Outline each uninfected red blood cell.
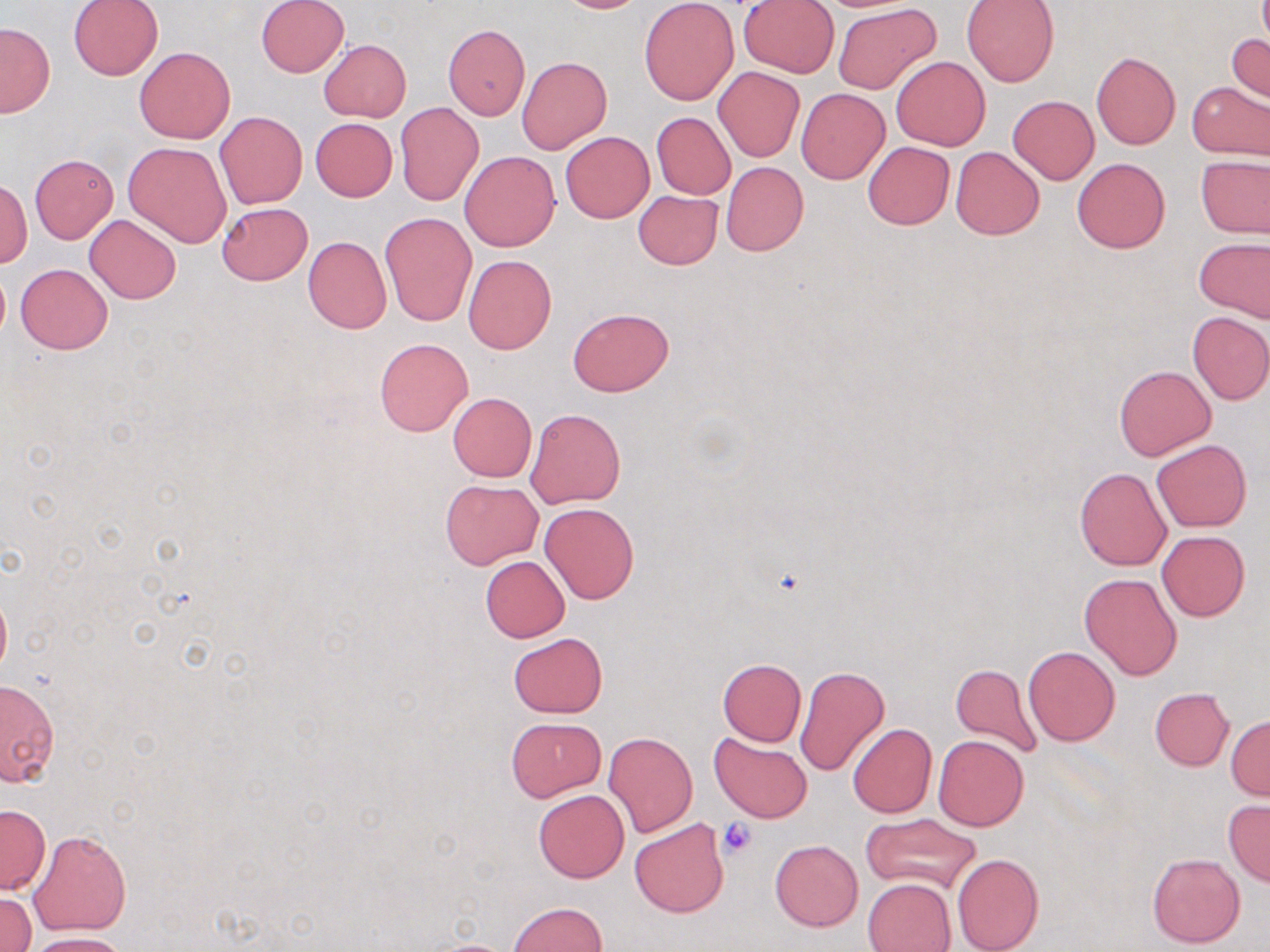
Approximate bounding boxes as (x1,y1)-(x2,y2) corner pairs in pixels.
Uninfected red blood cells: (68,0)-(163,80), (256,0)-(349,78), (547,0)-(650,13), (639,0)-(739,104), (738,1)-(839,78), (961,1)-(1059,87), (833,3)-(941,95), (0,22)-(54,119), (443,24)-(530,119), (1228,33)-(1269,103), (319,39)-(411,121), (134,47)-(235,144), (1091,52)-(1181,149), (517,56)-(612,155), (891,56)-(990,151), (713,66)-(804,161), (1186,81)-(1270,161), (796,87)-(890,184), (1007,95)-(1099,183), (395,102)-(484,206), (213,111)-(308,210), (651,113)-(735,199), (310,118)-(397,200), (560,132)-(654,223), (125,141)-(232,246), (863,142)-(955,230), (951,147)-(1044,239), (460,151)-(560,252), (1196,154)-(1270,239), (30,155)-(118,243), (1071,157)-(1170,253), (721,162)-(808,256), (1,181)-(31,268), (633,190)-(723,269), (216,201)-(312,285), (380,213)-(477,326), (85,214)-(181,304), (304,236)-(392,334), (1194,237)-(1270,322), (463,255)-(556,354), (16,264)-(112,354), (0,267)-(10,341), (568,308)-(674,396), (1187,310)-(1270,405), (374,336)-(473,436), (1114,365)-(1216,459), (448,392)-(537,482), (525,408)-(626,508), (1152,439)-(1252,531), (1074,466)-(1171,571), (441,479)-(542,569), (539,502)-(639,604), (1157,530)-(1249,621), (480,556)-(571,642), (1080,572)-(1183,681), (0,587)-(11,679), (509,632)-(607,718), (1024,646)-(1120,746), (718,658)-(806,747), (950,663)-(1041,758), (794,666)-(891,778), (0,678)-(58,787), (1150,688)-(1234,770), (1227,716)-(1270,799), (506,717)-(606,801), (848,723)-(937,818), (603,732)-(699,837), (932,734)-(1029,831), (710,735)-(812,823), (533,790)-(630,883), (1223,800)-(1270,886), (1,803)-(50,895), (861,814)-(980,893), (630,818)-(729,918), (29,828)-(131,936), (770,839)-(863,930), (952,852)-(1044,952), (1147,852)-(1246,948), (863,878)-(956,952), (2,891)-(34,952), (507,902)-(607,952), (25,933)-(129,952).

Platelet locations: (716,818)-(758,858). Slide-level diagnosis: no evidence of blood parasites. May-Grünwald-Giemsa-stained preparation. Light microscopy. Single field of view. 1000x magnification. Thin blood smear. Image is 1270×952 pixels.